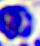

A leukocyte is shown. Micrograph. 400x magnification.